Evaluate for Plasmodium parasites.
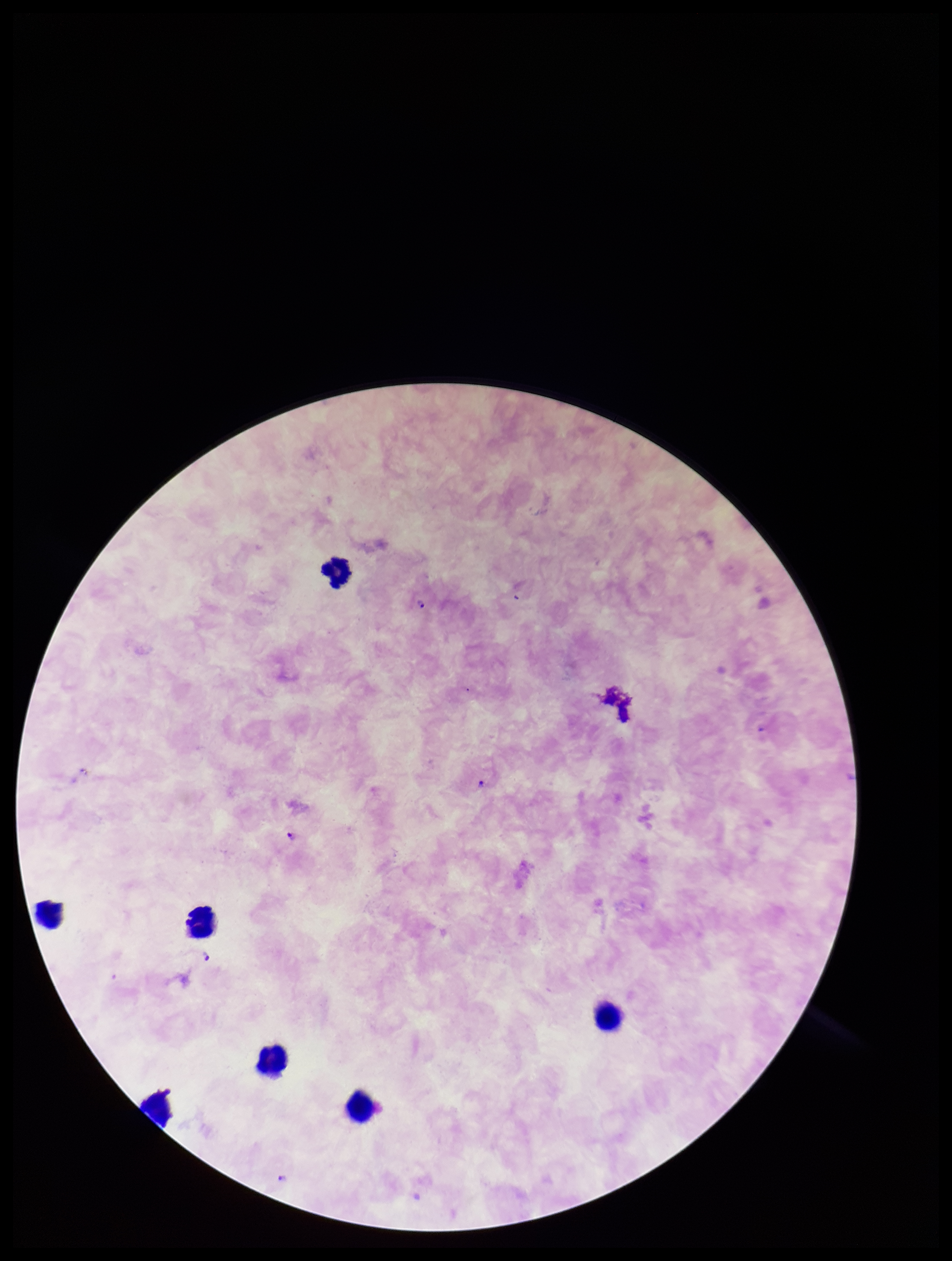
Detected.

species_reported_for_this_patient: Plasmodium falciparum
preparation: thick blood smear
capture: smartphone photograph through the microscope eyepiece
field_of_view: single
patient_malaria_status: positive
stain: Giemsa
parasite_count: 6
image_size: 952×1261 pixels
leukocyte_count: 7